Assess this cell for malaria.
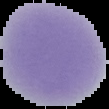
It is uninfected.

Image is 109×109 pixels. From a thin blood film. Segmented cell region on a black background.